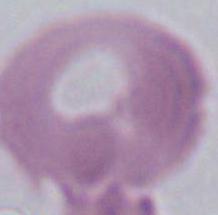

Summary:
  - Modality: photomicrograph
  - Identification: erythrocyte
  - Magnification: 1000x